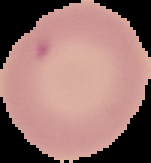
{
  "preparation": "thin blood film",
  "image_type": "cell region segmented out of the field of view; surrounding area masked to black",
  "image_size": "151×163 pixels",
  "result": "negative for Plasmodium parasites"
}